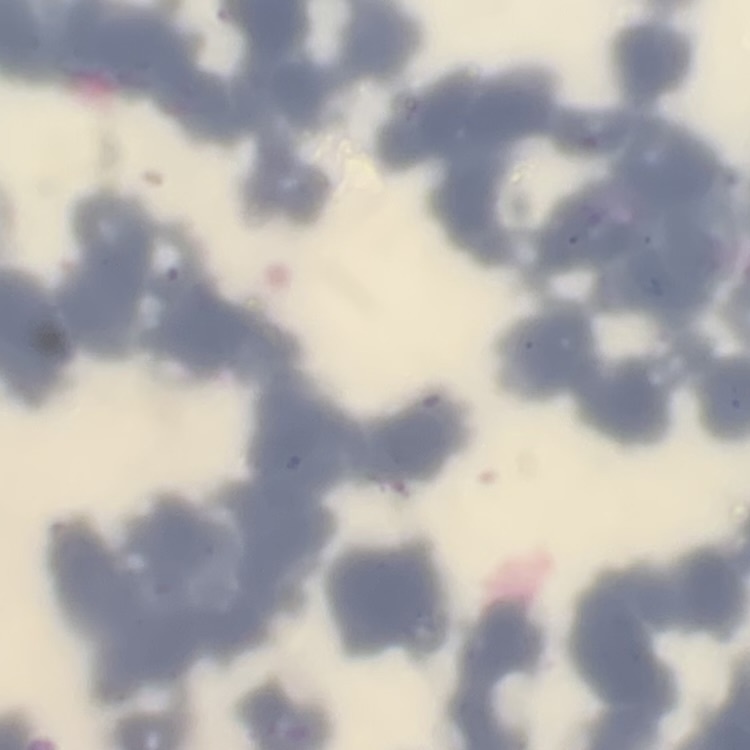
{
  "red_blood_cell_morphology": "rouleaux formation",
  "preparation": "thin peripheral smear",
  "stain": "Field's or Giemsa",
  "image_type": "square crop of a larger photomicrograph"
}